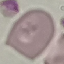
Summary:
  - Result: no malaria parasites seen
  - Image type: automatically extracted cell patch, resized to 64 × 64 pixels
  - Stain: Giemsa
  - Capture: smartphone through the microscope eyepiece
  - Preparation: thin blood film